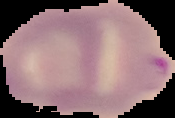

image_size: 175×118 pixels
preparation: thin blood film
malaria_status: parasitized
image_type: segmented cell region on a black background